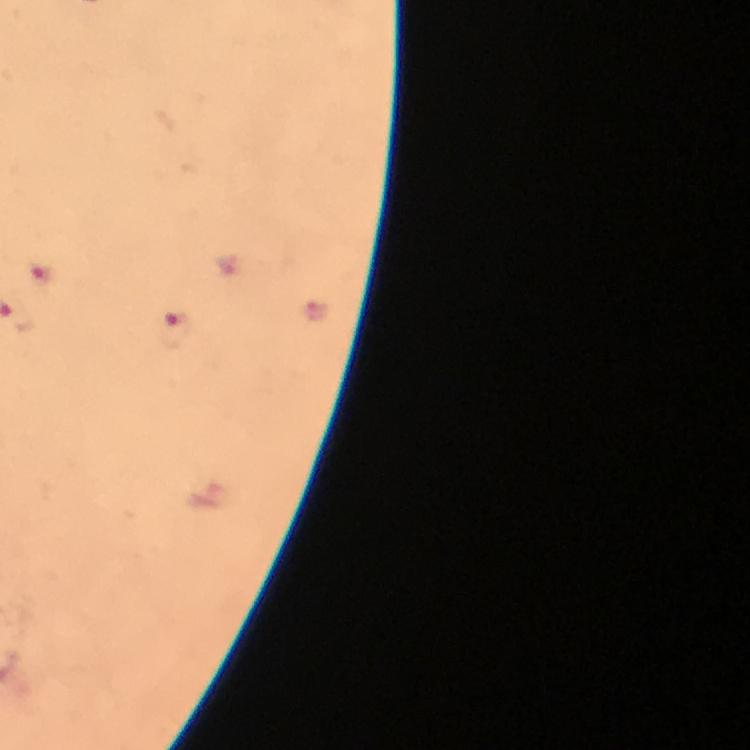
Approximate object centers, in pixels from the top-left corner. Malaria parasite locations: (x=40, y=274), (x=173, y=330). From a diagnostic examination for malaria. Smartphone photograph taken through a microscope. Immersion oil was used. Thick blood smear. Cropped region of a single field of view. 100x magnification. Image is 750×750 pixels. Giemsa-stained preparation.